Report the malaria status of this cell.
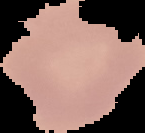

Uninfected.

Summary:
  - Image size: 145×133 pixels
  - Preparation: thin blood film
  - Image type: segmented cell region on a black background